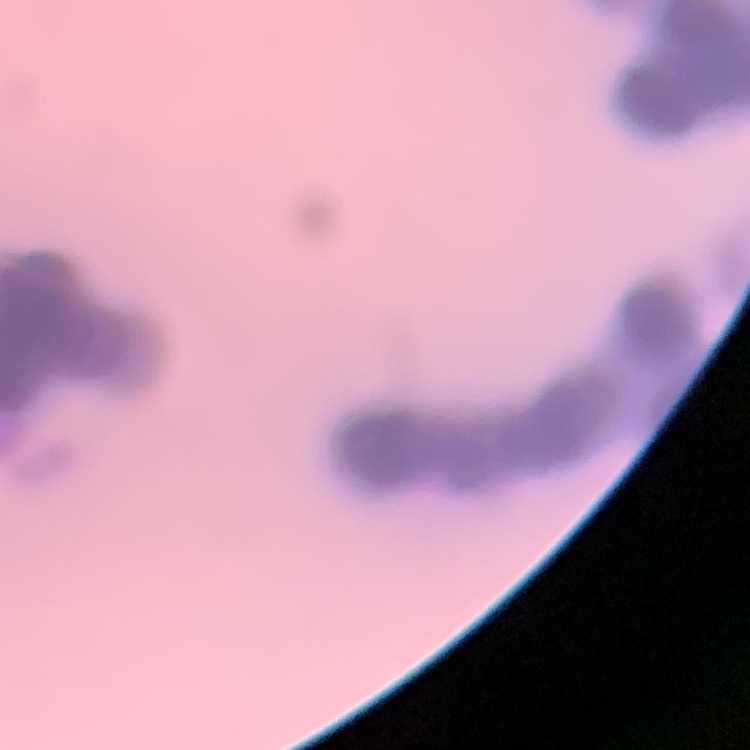

The erythrocytes exhibit rouleaux formation. Thin blood film. Square crop of a larger photomicrograph. Field's or Giemsa stain.